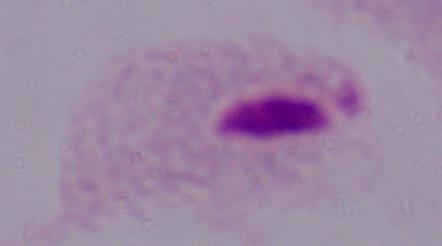
{
  "modality": "photomicrograph",
  "identification": "trichomonad",
  "magnification": "1000x"
}